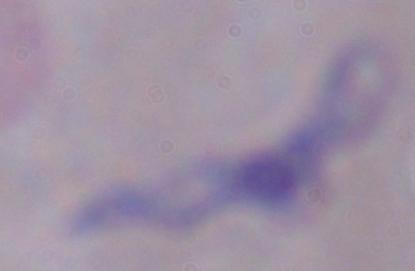
Summary:
  - Modality: photomicrograph
  - Identification: trypanosome
  - Magnification: 1000x